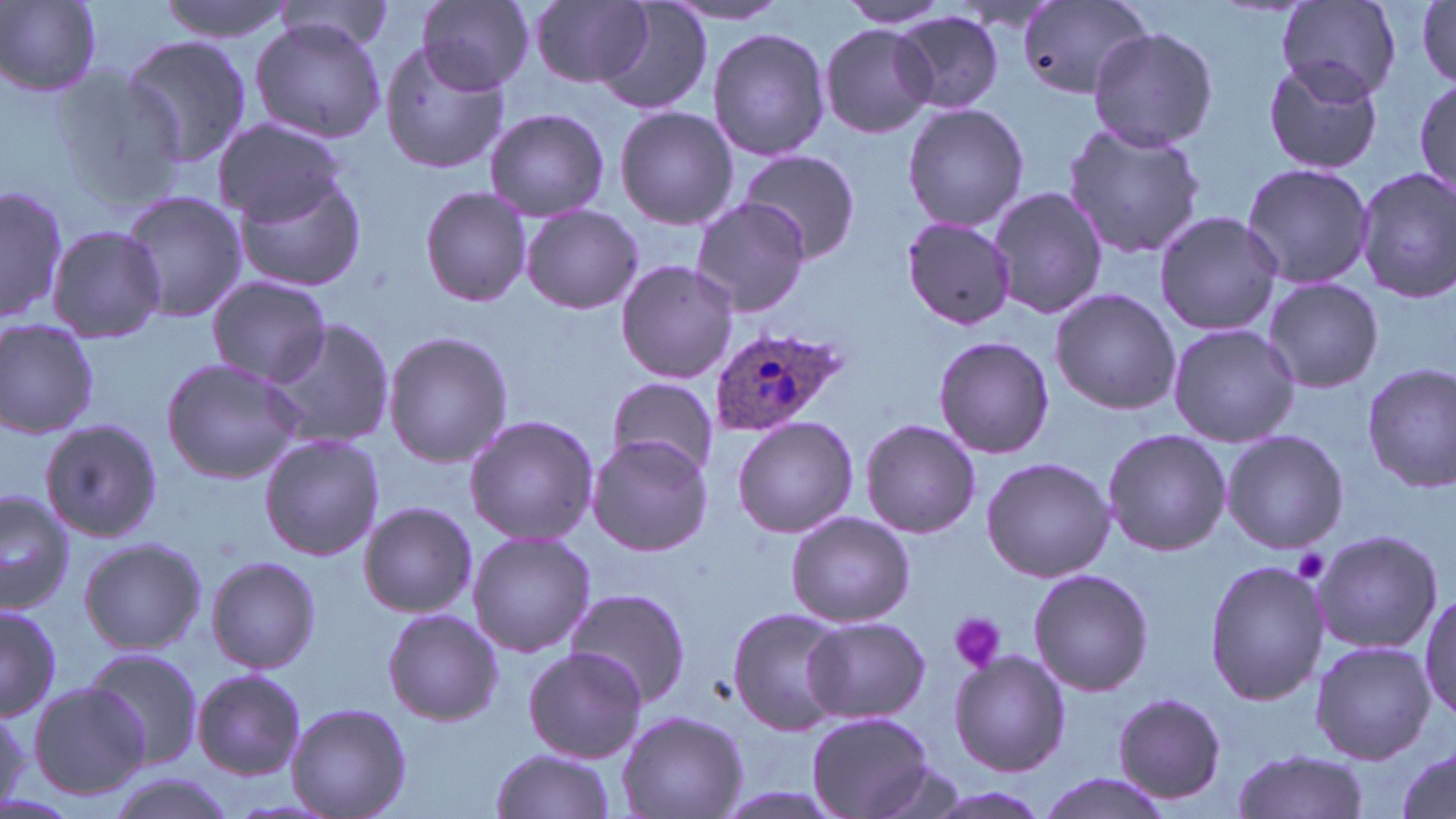

Approximate bounding boxes as [x1, y1, x2, y2] in pixels. Platelet locations: [1293, 547, 1333, 584], [948, 613, 1005, 672]. Uninfected red blood cell locations: [1, 0, 102, 96], [156, 0, 296, 43], [414, 0, 537, 94], [834, 0, 954, 29], [1279, 0, 1403, 100], [1415, 0, 1455, 88], [531, 1, 656, 88], [1017, 1, 1149, 100], [274, 2, 396, 51], [596, 2, 714, 117], [668, 2, 794, 24], [893, 12, 1005, 115], [249, 19, 384, 143], [819, 23, 937, 136], [1089, 25, 1217, 152], [707, 27, 831, 160], [120, 35, 254, 169], [380, 42, 511, 174], [1262, 57, 1385, 174], [48, 65, 190, 206], [1412, 72, 1455, 203], [901, 101, 1029, 233], [615, 105, 738, 230], [484, 107, 610, 222], [213, 118, 346, 225], [1062, 121, 1207, 258], [736, 149, 863, 265], [1238, 161, 1374, 288], [1355, 168, 1456, 304], [233, 171, 367, 292], [1, 184, 68, 326], [420, 185, 533, 309], [987, 186, 1106, 321], [118, 191, 247, 322], [690, 198, 811, 315], [521, 205, 641, 314], [1153, 209, 1284, 336], [902, 217, 1018, 329], [48, 225, 166, 345], [615, 260, 739, 384], [208, 275, 333, 385], [1262, 278, 1384, 392], [1049, 288, 1180, 417], [261, 317, 396, 450], [0, 320, 99, 439], [1166, 322, 1298, 447], [382, 330, 513, 469], [933, 335, 1055, 460], [160, 357, 303, 485], [1363, 363, 1456, 492], [606, 376, 722, 477], [464, 415, 599, 546], [732, 416, 858, 538], [42, 417, 165, 540], [860, 418, 981, 536], [1102, 428, 1232, 557], [1221, 429, 1349, 553], [259, 432, 384, 562], [588, 434, 712, 555], [980, 456, 1116, 583], [0, 489, 77, 613], [358, 501, 478, 618], [785, 510, 914, 627], [1311, 528, 1444, 654], [467, 531, 595, 658], [78, 536, 207, 655], [206, 556, 321, 675], [1205, 560, 1327, 706], [1030, 568, 1152, 697], [563, 586, 691, 709], [1417, 590, 1455, 723], [0, 603, 61, 721], [382, 607, 505, 725], [726, 607, 849, 736], [802, 616, 932, 724], [1311, 640, 1433, 763], [79, 646, 205, 769], [521, 647, 648, 764], [949, 650, 1070, 776], [192, 668, 307, 779], [26, 682, 152, 801], [1112, 693, 1229, 805], [287, 701, 411, 819], [0, 705, 29, 808], [617, 708, 747, 819], [807, 713, 937, 819], [488, 748, 617, 819], [1230, 748, 1368, 819], [1394, 749, 1455, 817], [863, 761, 969, 818], [99, 771, 239, 819], [1034, 773, 1173, 819], [916, 786, 1053, 819]. Plasmodium ovale-infected red blood cell locations: [707, 327, 846, 437]. Slide-level diagnosis: Plasmodium ovale. Image is 1456×819 pixels. Thin blood smear. May-Grünwald-Giemsa stain. 1000x magnification. Single field of view. Light microscopy.